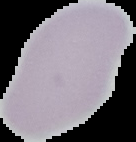
Image is 136×142 pixels. Result: no malaria parasites seen. From a thin blood smear. The area outside the segmented cell region is set to black.